Identify the preparation type.
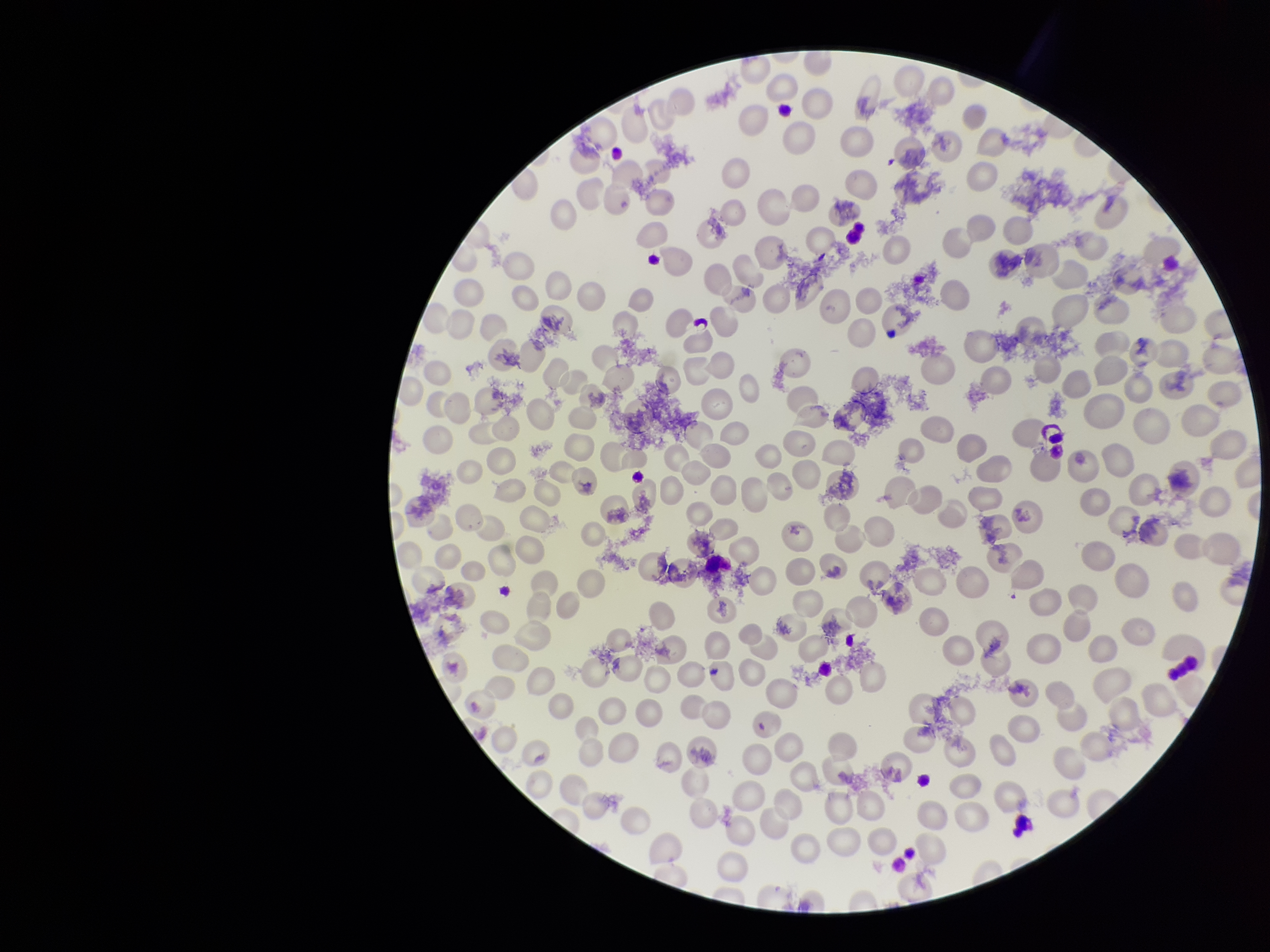

A thin smear.

{
  "capture": "smartphone photograph through the microscope eyepiece",
  "patient_malaria_status": "negative",
  "field_of_view": "single",
  "stain": "Giemsa",
  "parasitized_red_blood_cell_count": 0,
  "red_blood_cell_count": 236,
  "parasitized_red_blood_cells": "none detected",
  "image_size": "1270×952 pixels"
}